Assess the morphology of the erythrocytes.
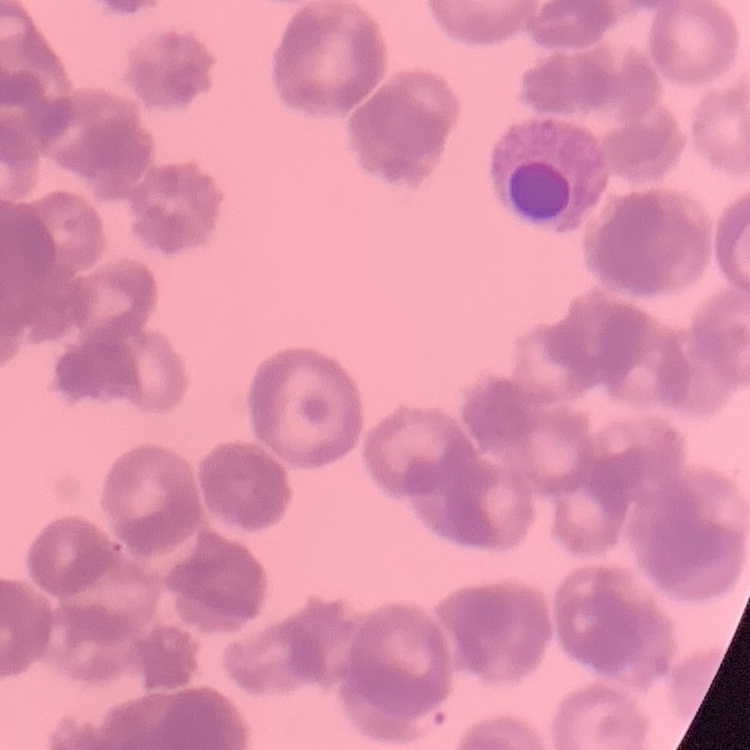

They show rouleaux formation.

image type = square crop of a larger photomicrograph
stain = Field's or Giemsa
preparation = thin blood film